Assess this cell for malaria.
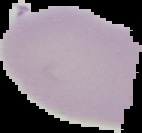
It is uninfected.

image_type: segmented cell region with the area outside set to black
image_size: 142×133 pixels
preparation: thin blood smear